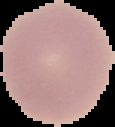
Summary:
  - Preparation: thin blood smear
  - Image type: segmented cell region on a black background
  - Result: no Plasmodium parasites detected
  - Image size: 115×127 pixels